Report the malaria status.
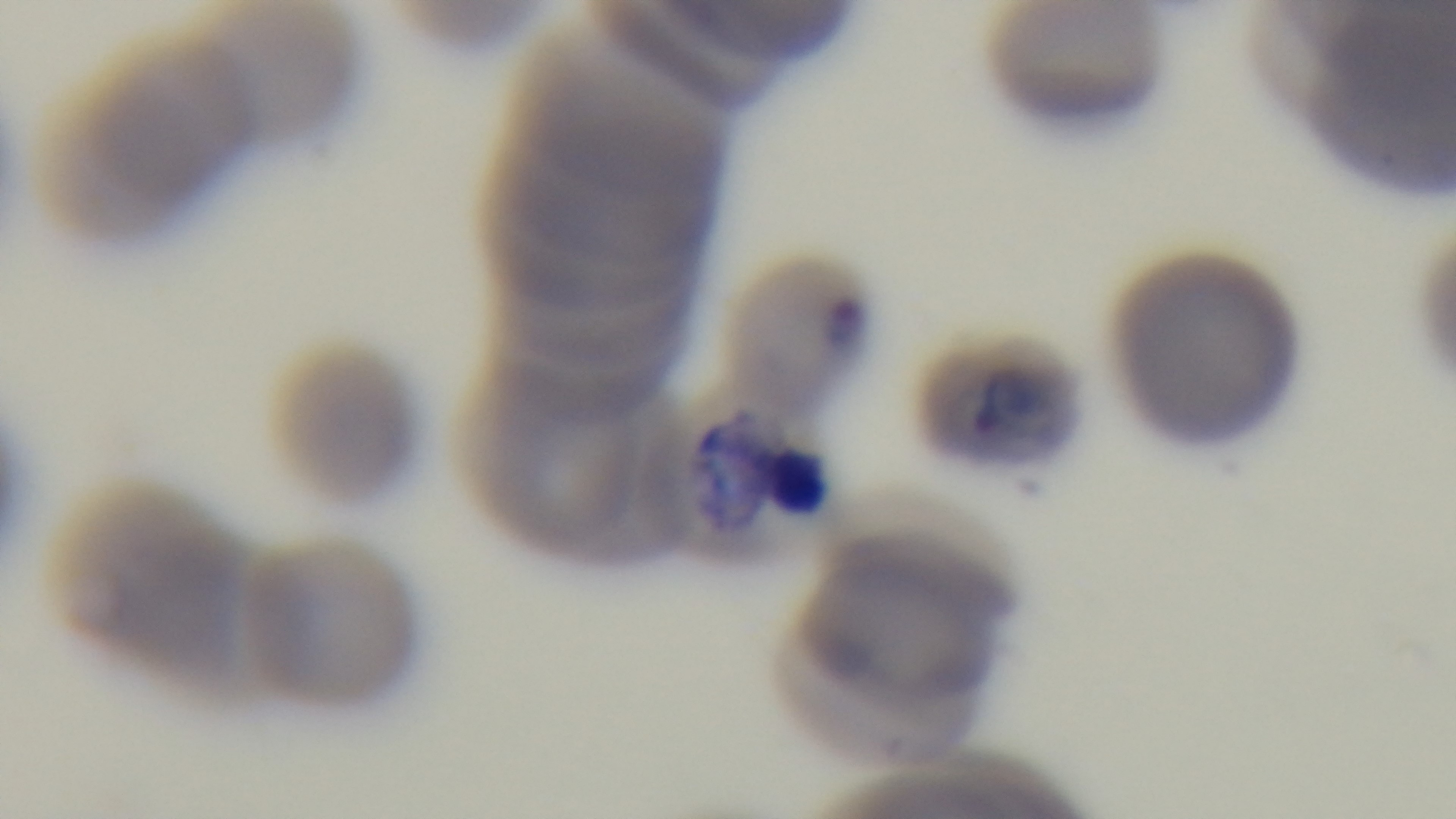
Positive.

{
  "capture": "mounted 4K digital camera",
  "preparation": "thin blood film",
  "field_of_view": "one from the slide",
  "stain": "Giemsa",
  "objective": "100x oil immersion",
  "modality": "light microscopy"
}